Assess the morphology of the erythrocytes.
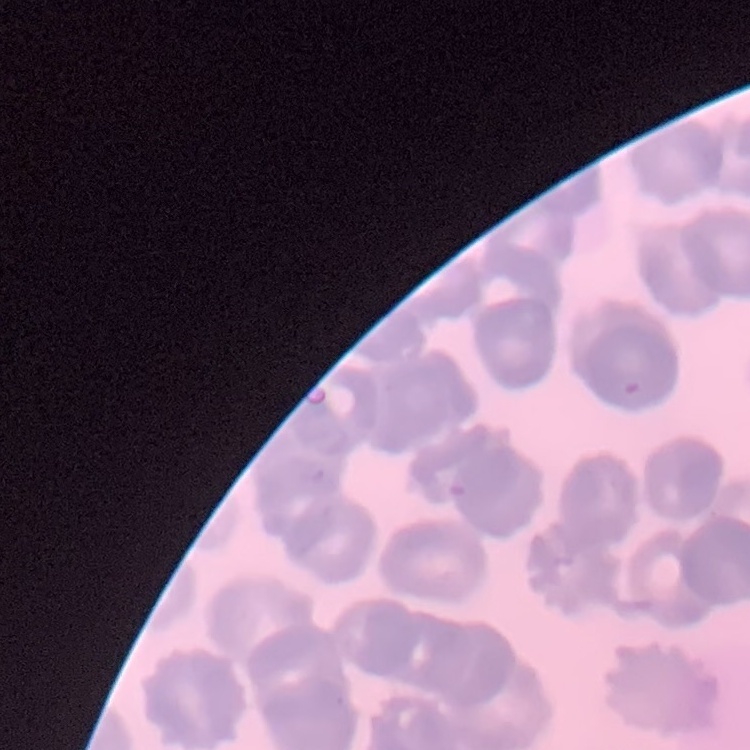
They show rouleaux formation.

Summary:
  - Preparation: thin peripheral smear
  - Stain: Field's or Giemsa
  - Image type: square crop of a larger photomicrograph